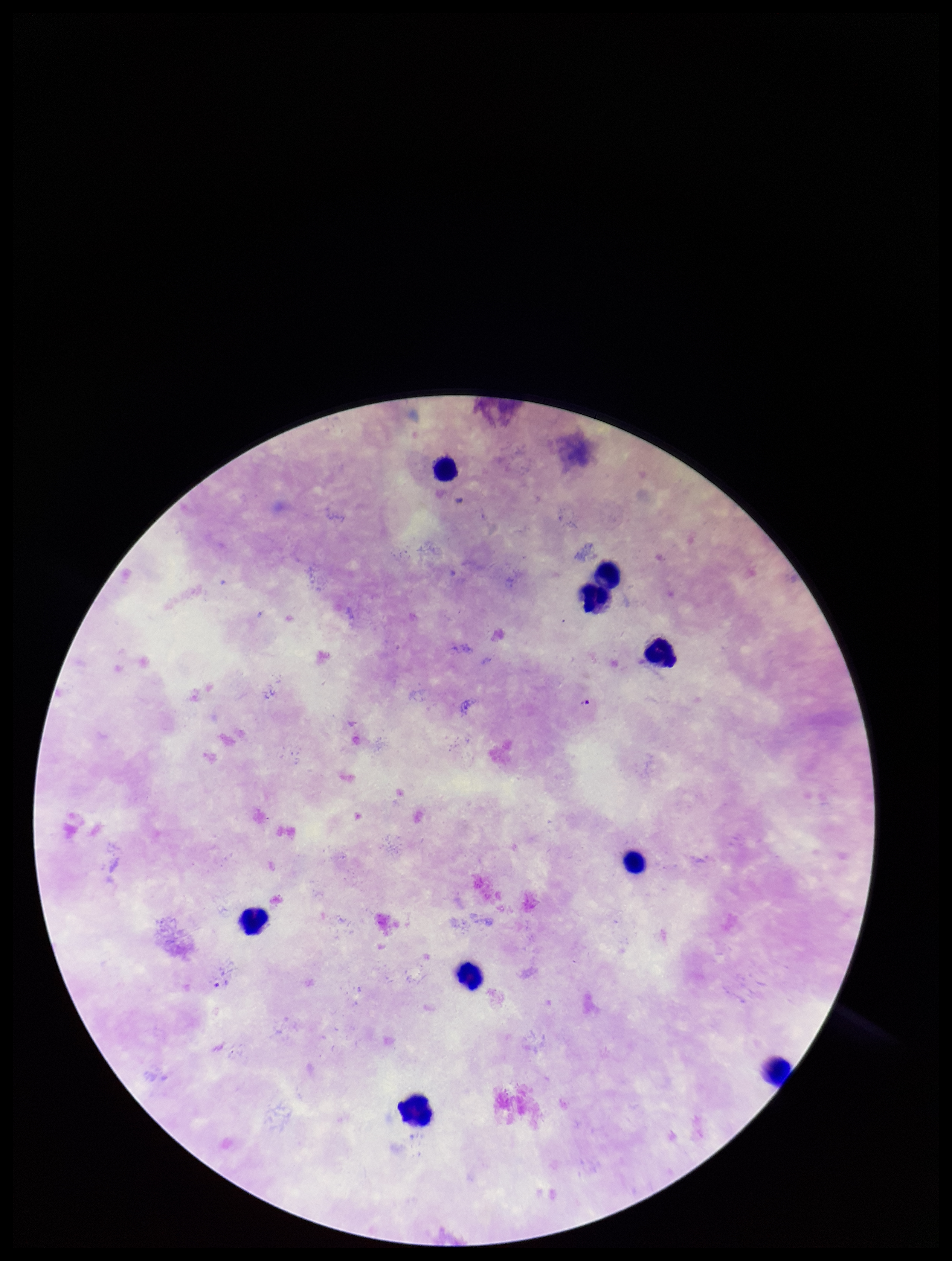
Summary:
  - Species reported for this patient: Plasmodium falciparum
  - Plasmodium parasites: detected
  - Image size: 952×1261 pixels
  - Preparation: thick blood smear
  - Leukocyte count: 9
  - Parasite count: 1
  - Capture: smartphone photograph through the microscope eyepiece
  - Patient malaria status: positive
  - Field of view: single
  - Stain: Giemsa